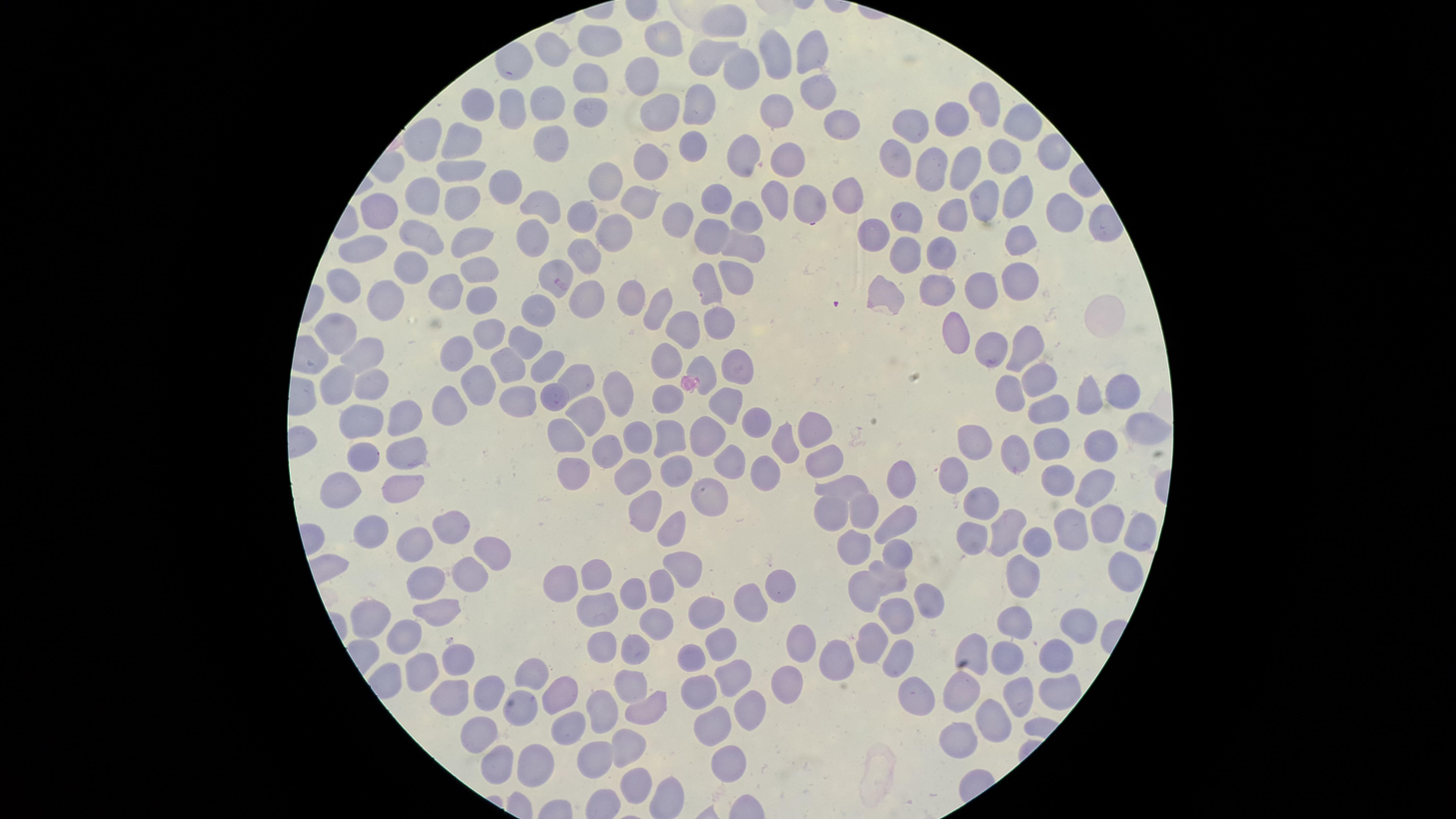
Approximate marker points, in pixels from the top-left corner. Parasitized red blood cells: (x=553, y=274). Uninfected red blood cells: (x=724, y=20), (x=669, y=39), (x=597, y=41), (x=556, y=53), (x=710, y=56), (x=784, y=56), (x=808, y=56), (x=740, y=64), (x=638, y=73), (x=584, y=78), (x=815, y=88), (x=543, y=103), (x=477, y=105), (x=510, y=105), (x=689, y=105), (x=988, y=105), (x=661, y=110), (x=780, y=110), (x=591, y=114), (x=951, y=115), (x=840, y=118), (x=911, y=123), (x=1017, y=128), (x=459, y=138), (x=551, y=139), (x=421, y=141), (x=690, y=145), (x=743, y=149), (x=1053, y=150), (x=897, y=155), (x=1003, y=156), (x=789, y=158), (x=654, y=160), (x=964, y=162), (x=929, y=167), (x=455, y=170), (x=606, y=183), (x=502, y=186), (x=843, y=191), (x=417, y=194), (x=1022, y=194), (x=773, y=197), (x=462, y=198), (x=985, y=198), (x=721, y=199), (x=809, y=201), (x=547, y=202), (x=636, y=204), (x=388, y=207), (x=957, y=210), (x=1063, y=210), (x=751, y=214), (x=588, y=217), (x=906, y=217), (x=619, y=228), (x=874, y=229), (x=533, y=230), (x=714, y=235), (x=1019, y=235), (x=414, y=238), (x=468, y=238), (x=367, y=242), (x=743, y=249), (x=904, y=249), (x=938, y=250), (x=581, y=256), (x=406, y=264), (x=484, y=265), (x=736, y=276), (x=1016, y=276), (x=450, y=282), (x=940, y=286), (x=706, y=288), (x=884, y=288), (x=977, y=288), (x=589, y=289), (x=342, y=291), (x=631, y=296), (x=386, y=298), (x=477, y=300), (x=653, y=309), (x=722, y=323), (x=686, y=325), (x=333, y=330), (x=957, y=331), (x=486, y=332), (x=524, y=338), (x=1024, y=342), (x=995, y=345), (x=367, y=351), (x=454, y=351), (x=665, y=360), (x=506, y=362), (x=700, y=364), (x=550, y=367), (x=737, y=368), (x=342, y=378), (x=573, y=378), (x=1036, y=379), (x=473, y=382), (x=370, y=384), (x=622, y=385), (x=1015, y=389), (x=518, y=394), (x=554, y=394), (x=669, y=394), (x=1126, y=394), (x=718, y=398), (x=449, y=400), (x=1092, y=403), (x=1050, y=407), (x=594, y=410), (x=396, y=417), (x=745, y=419), (x=362, y=420), (x=803, y=420), (x=1147, y=422), (x=573, y=431), (x=707, y=434), (x=630, y=435), (x=671, y=436), (x=784, y=437), (x=980, y=437), (x=1097, y=441), (x=1054, y=442), (x=1010, y=447), (x=403, y=449), (x=607, y=449), (x=363, y=454), (x=736, y=456), (x=831, y=459), (x=638, y=470), (x=678, y=470), (x=765, y=470), (x=952, y=472), (x=567, y=480), (x=1055, y=480), (x=900, y=484), (x=1096, y=485), (x=850, y=487), (x=403, y=488), (x=347, y=491), (x=712, y=495), (x=978, y=499), (x=640, y=506), (x=862, y=510), (x=829, y=512), (x=1008, y=523), (x=1106, y=523), (x=897, y=524), (x=1069, y=524), (x=453, y=526), (x=969, y=532), (x=1045, y=534), (x=378, y=535), (x=673, y=536), (x=1135, y=536), (x=415, y=540), (x=856, y=545), (x=488, y=548), (x=898, y=549), (x=681, y=567), (x=459, y=570), (x=1120, y=570), (x=594, y=573), (x=1024, y=573), (x=888, y=576), (x=561, y=578), (x=784, y=584), (x=662, y=585), (x=422, y=589), (x=861, y=591), (x=638, y=593), (x=751, y=603), (x=921, y=603), (x=597, y=607), (x=431, y=613), (x=704, y=613), (x=373, y=615), (x=887, y=616), (x=655, y=619), (x=1077, y=621), (x=1018, y=625), (x=410, y=634), (x=722, y=643), (x=867, y=643), (x=636, y=645), (x=794, y=645), (x=973, y=645), (x=601, y=646), (x=896, y=652), (x=692, y=658), (x=833, y=658), (x=1047, y=659), (x=454, y=660), (x=1010, y=662), (x=534, y=671), (x=423, y=673), (x=736, y=674), (x=782, y=681), (x=628, y=682), (x=699, y=688), (x=454, y=692), (x=964, y=692), (x=1052, y=692), (x=485, y=693), (x=563, y=695), (x=912, y=695), (x=1022, y=697), (x=522, y=705), (x=744, y=706), (x=647, y=707), (x=595, y=710), (x=1002, y=718), (x=570, y=724), (x=714, y=724), (x=482, y=732), (x=958, y=739), (x=633, y=742), (x=596, y=756), (x=491, y=758), (x=533, y=758), (x=727, y=758), (x=632, y=784). Photographed with a smartphone camera through the microscope eyepiece. Species: Plasmodium falciparum. Thin smear of blood. Single field of view. Presence: malaria parasites detected. The visible region is circular. Image is 1456×819 pixels. Giemsa stain.